Identify the parasite.
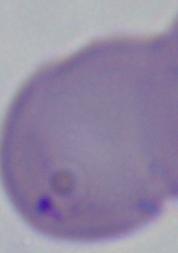
Babesia.

Summary:
  - Modality: photomicrograph
  - Magnification: 1000x